Give the extent of all Plasmodium ovale-infected red blood cells.
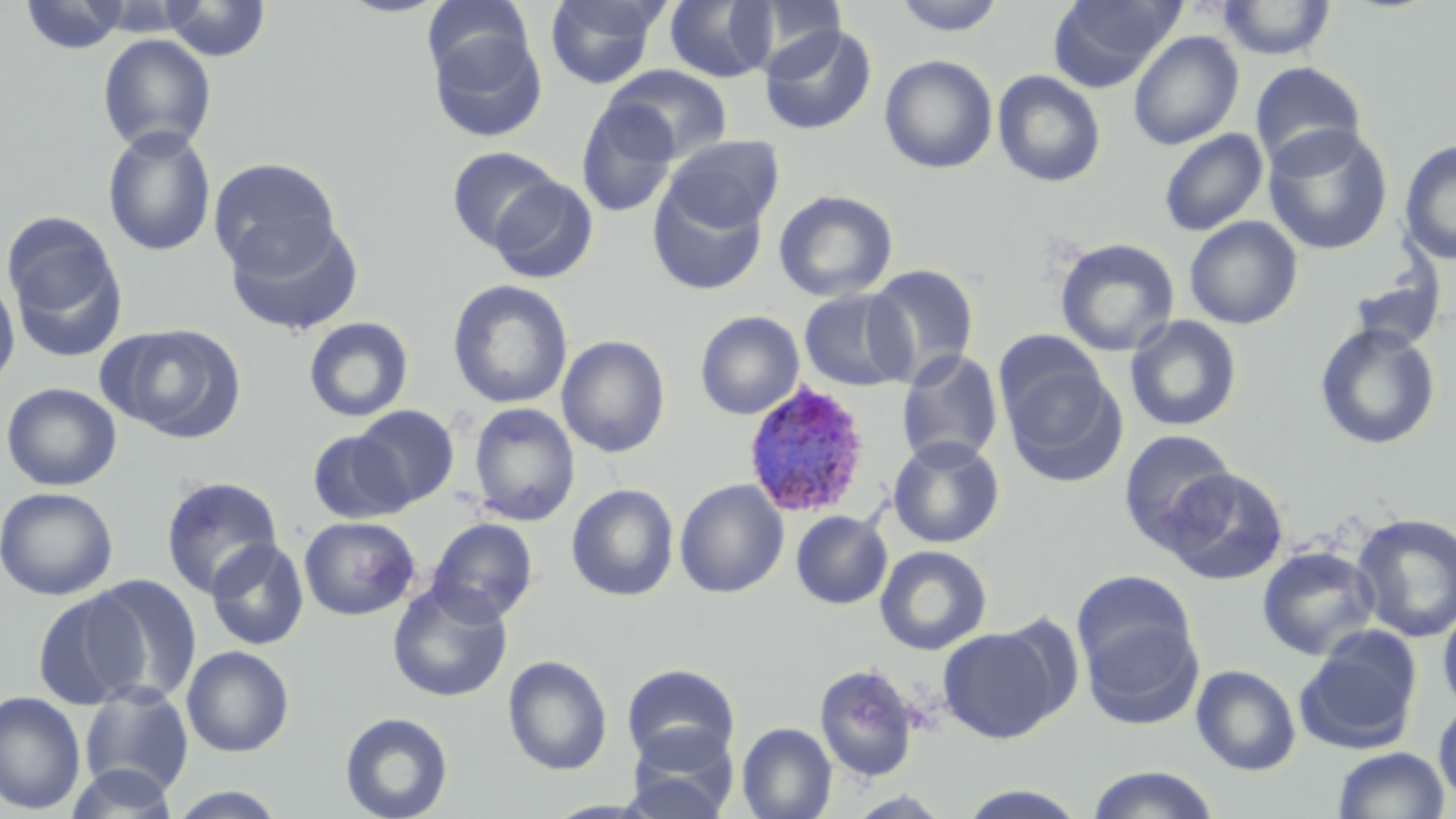
Approximate bounding boxes as (x1, y1, x2, y2) in pixels.
Plasmodium ovale-infected red blood cells: (742, 383, 873, 519).

Uninfected red blood cell locations: (19, 0, 131, 54), (159, 0, 271, 61), (544, 0, 667, 89), (746, 0, 848, 71), (891, 0, 1007, 36), (1048, 0, 1185, 91), (421, 1, 535, 85), (663, 1, 778, 83), (1216, 1, 1338, 60), (759, 23, 877, 136), (427, 28, 547, 143), (1128, 30, 1244, 151), (98, 34, 216, 155), (879, 54, 998, 174), (1250, 61, 1367, 172), (606, 65, 734, 163), (992, 70, 1107, 187), (576, 96, 680, 218), (102, 125, 217, 257), (1263, 126, 1394, 255), (1159, 128, 1268, 237), (662, 135, 784, 234), (1398, 140, 1456, 265), (446, 146, 562, 251), (207, 157, 342, 274), (486, 176, 598, 284), (648, 182, 768, 296), (773, 189, 898, 302), (2, 211, 129, 362), (224, 215, 365, 337), (1184, 216, 1304, 329), (1054, 238, 1180, 357), (865, 264, 979, 383), (1347, 267, 1445, 352), (0, 274, 20, 398), (447, 279, 573, 409), (798, 288, 916, 392), (695, 311, 804, 420), (1124, 315, 1244, 433), (303, 316, 414, 422), (104, 323, 247, 443), (1314, 323, 1441, 450), (556, 335, 671, 458), (896, 349, 1003, 467), (999, 354, 1127, 486), (0, 382, 122, 491), (468, 403, 580, 526), (352, 405, 460, 510), (1118, 429, 1238, 552), (307, 430, 410, 524), (887, 436, 1006, 548), (1161, 467, 1289, 585), (160, 475, 284, 599), (674, 479, 789, 598), (567, 483, 680, 601), (0, 487, 119, 600), (791, 510, 892, 609), (1351, 512, 1456, 643), (299, 516, 420, 620), (427, 517, 538, 624), (206, 538, 310, 651), (874, 544, 992, 656), (1256, 544, 1380, 661), (1071, 569, 1198, 681), (85, 574, 203, 705), (387, 581, 513, 703), (33, 589, 149, 709), (1437, 601, 1456, 717), (1081, 617, 1204, 729), (937, 624, 1066, 743), (1295, 630, 1422, 755), (181, 645, 295, 757), (503, 655, 613, 776), (814, 663, 921, 782), (621, 664, 740, 768), (1191, 664, 1302, 776), (79, 684, 194, 796), (0, 691, 86, 815), (1433, 699, 1456, 805), (340, 711, 453, 819), (737, 723, 837, 819), (623, 730, 739, 819), (1331, 746, 1450, 819), (66, 763, 180, 818), (1086, 765, 1221, 819), (956, 783, 1090, 818), (167, 786, 289, 818). Slide-level diagnosis: Plasmodium ovale. Single field of view. Image is 1456×819 pixels. Light microscopy. May-Grünwald-Giemsa stain. 1000x magnification. Thin blood smear.